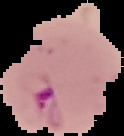
Summary:
  - Malaria status: parasitized
  - Image type: cell region segmented out of the field of view; surrounding area masked to black
  - Image size: 124×136 pixels
  - Preparation: thin blood film